Classify this cell by malaria status.
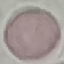
It is uninfected.

image_type: cell patch, automatically extracted from a larger field of view and resized to 64 × 64 pixels
capture: smartphone through the microscope eyepiece
preparation: thin blood film
stain: Giemsa